Name the parasite shown.
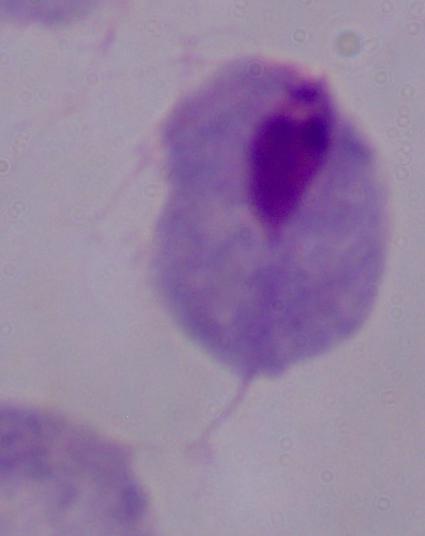

A trichomonad.

Summary:
  - Modality: micrograph
  - Magnification: 1000x